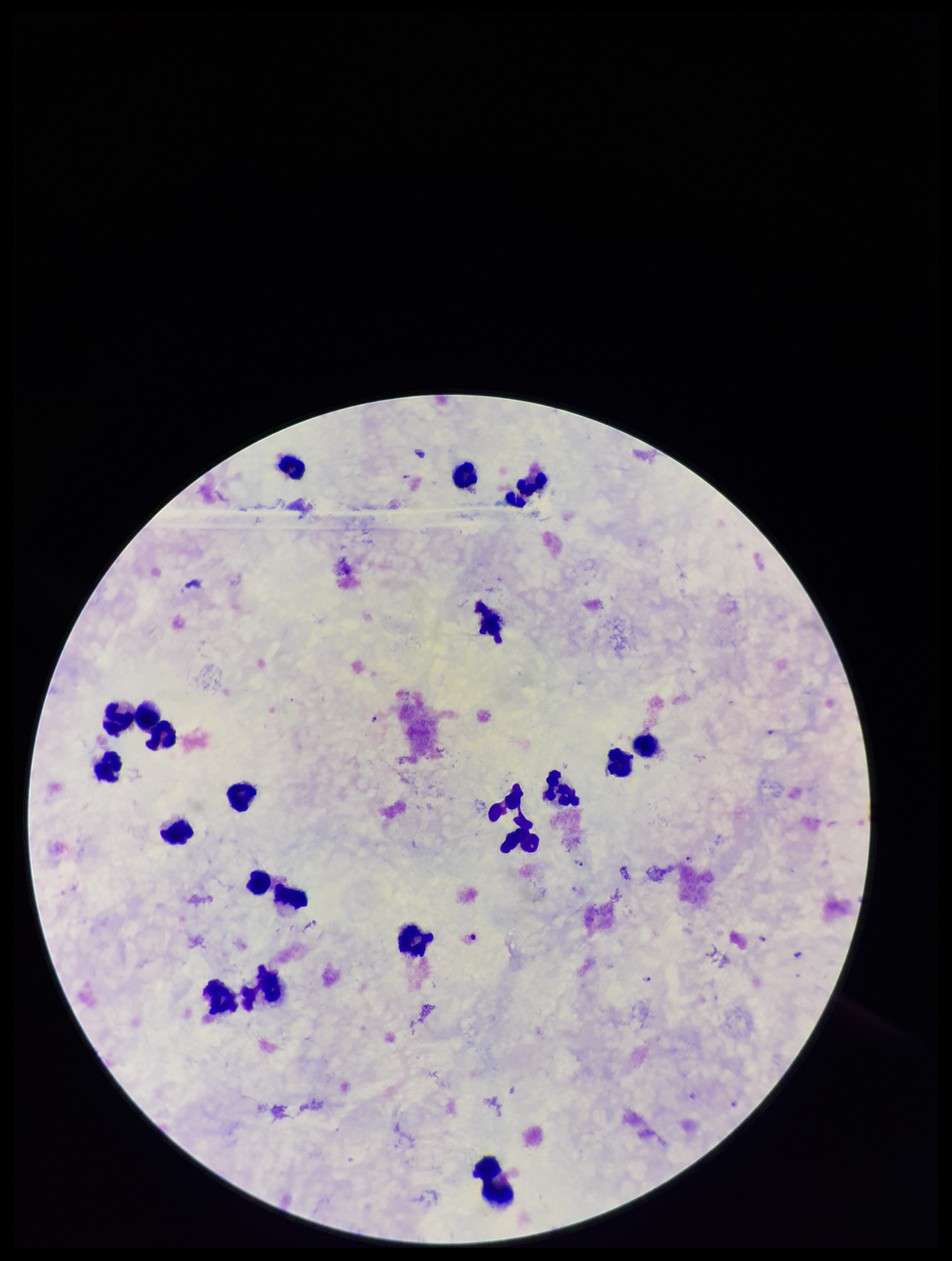
Image is 952×1261 pixels. Patient malaria status: positive. Species reported for this patient: Plasmodium falciparum. Preparation: thick smear. Leukocyte count: 21. Plasmodium parasites: identified. Single field of view. Parasite count: 5. Giemsa stain. Smartphone photograph taken through the eyepiece of a microscope.